Assess the morphology of the red blood cells.
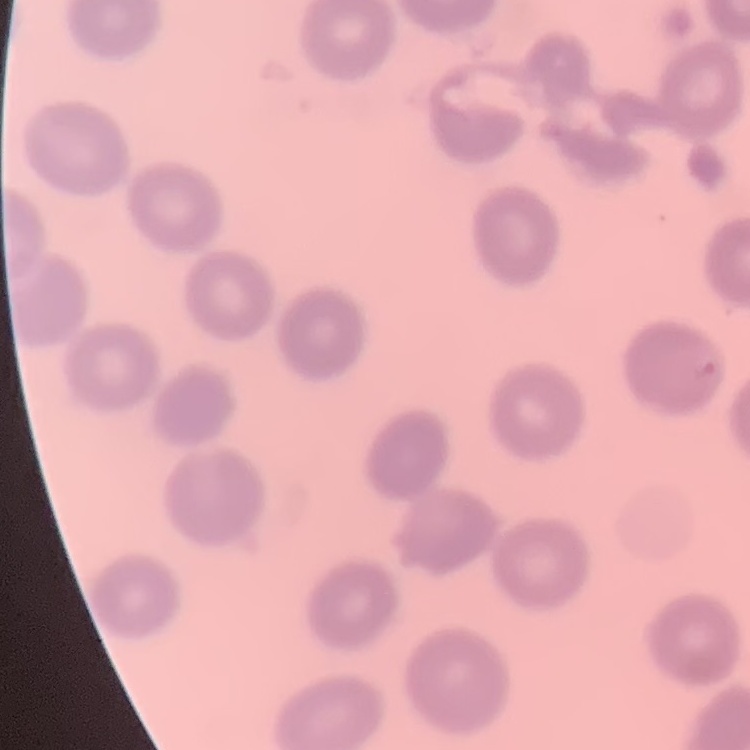
No rouleaux formation.

Summary:
  - Image type: one tile cut from a larger photomicrograph
  - Preparation: thin peripheral smear
  - Stain: Field's or Giemsa